Assess this cell for malaria.
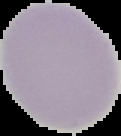

It is uninfected.

Summary:
  - Preparation: thin blood smear
  - Image size: 121×136 pixels
  - Image type: segmented cell region with the area outside set to black